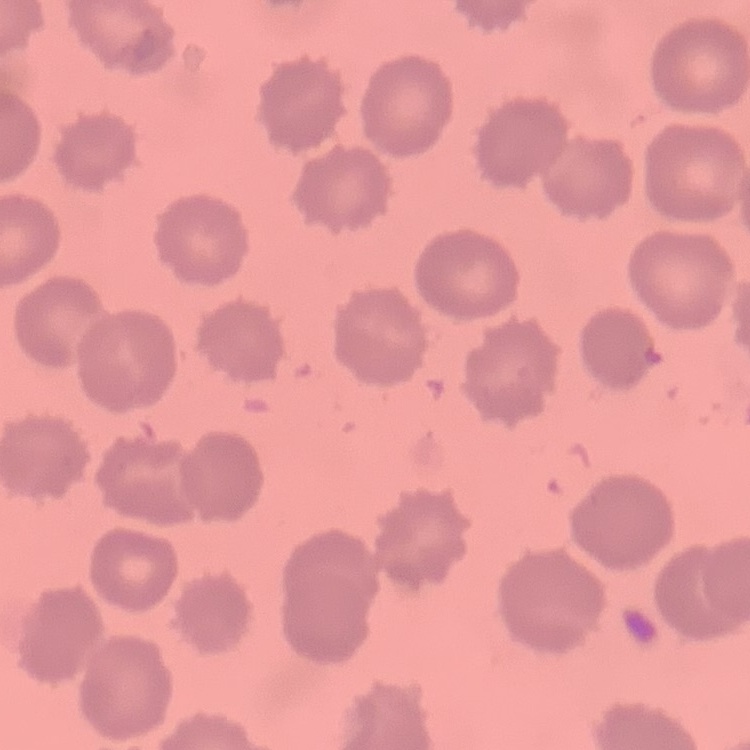
red blood cell morphology = no rouleaux formation
image type = square crop of a larger photomicrograph
stain = Field's or Giemsa
preparation = thin peripheral smear